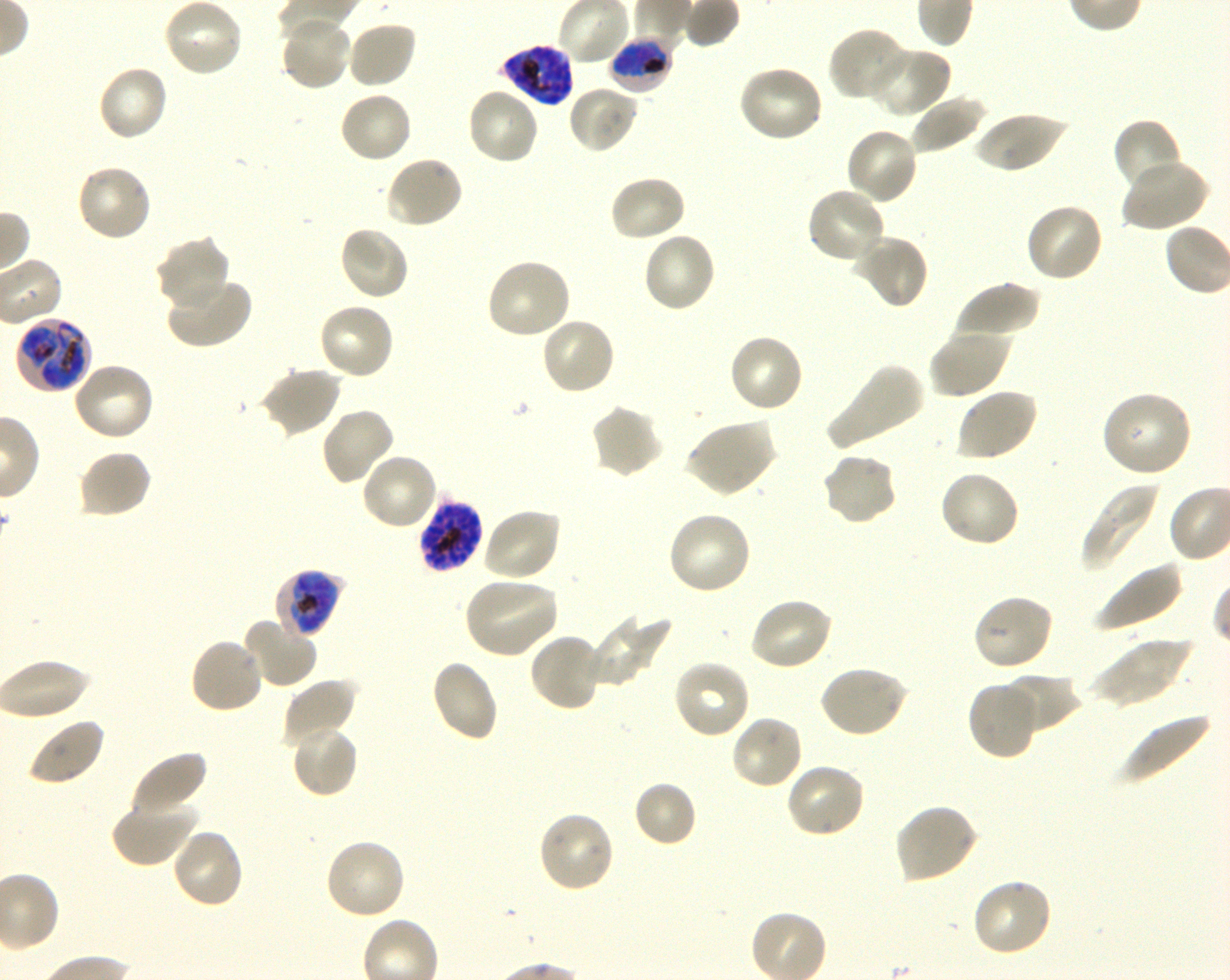
Approximate bounding boxes as (x1, y1, x2, y2) in pixels. Not every red blood cell is marked. A life-cycle stage — or a range of stages, where the recorded stages span more than one — follows each staged infected red blood cell. Locations of infected red blood cells: (608, 36, 674, 94) early trophozoite to early schizont; (498, 45, 574, 106) late trophozoite to late schizont; (14, 316, 93, 395) trophozoite; (419, 497, 482, 576) early trophozoite to late schizont; (274, 568, 346, 640) late trophozoite to early schizont. Locations of uninfected red blood cells: (162, 0, 244, 79), (278, 17, 352, 92), (345, 20, 417, 90), (828, 27, 910, 103), (865, 47, 951, 118), (737, 63, 825, 143), (96, 64, 169, 143), (567, 84, 639, 155), (466, 86, 540, 165), (339, 91, 414, 164), (909, 94, 987, 155), (973, 110, 1066, 175), (1112, 118, 1185, 194), (845, 126, 919, 205), (384, 154, 464, 229), (1120, 160, 1209, 233), (75, 163, 152, 242), (608, 174, 687, 244), (805, 187, 887, 266), (1024, 201, 1105, 283), (337, 225, 411, 302), (641, 232, 718, 314), (851, 233, 930, 310), (154, 235, 230, 314), (485, 258, 573, 341), (166, 275, 253, 350), (953, 282, 1041, 345), (317, 301, 396, 380), (540, 317, 617, 396), (928, 326, 1010, 399), (727, 333, 805, 414), (72, 361, 156, 442), (824, 363, 925, 450), (258, 367, 341, 437), (954, 387, 1039, 462), (1100, 390, 1194, 477), (589, 403, 664, 479), (320, 406, 397, 487), (684, 417, 776, 497), (76, 448, 152, 519), (820, 451, 898, 528), (360, 452, 439, 532), (938, 469, 1021, 549), (1081, 480, 1162, 570), (481, 506, 562, 583), (666, 511, 753, 596), (1094, 560, 1184, 634), (463, 578, 560, 659), (972, 593, 1054, 672), (748, 596, 834, 671), (586, 613, 672, 688), (245, 620, 318, 689), (528, 631, 606, 711), (189, 636, 265, 715), (1091, 636, 1195, 709), (430, 658, 500, 743), (0, 659, 95, 721), (672, 659, 751, 740), (818, 664, 909, 739), (1001, 672, 1081, 734), (280, 678, 358, 747), (967, 680, 1042, 760), (1120, 712, 1215, 786), (729, 713, 805, 790), (27, 715, 106, 786), (289, 722, 360, 799), (130, 750, 208, 818), (784, 761, 867, 839), (632, 780, 697, 848), (110, 795, 198, 868), (893, 803, 978, 884), (536, 809, 615, 894), (171, 826, 246, 909), (323, 837, 408, 921), (971, 876, 1054, 958). Image is 1230×980 pixels. Giemsa stain. Blood group of the donor: O+. Plasmodium falciparum strain 3D7 maintained in shaking in-vitro culture. Thin blood smear. Single field of view. 100x oil-immersion objective, numerical aperture 1.30.